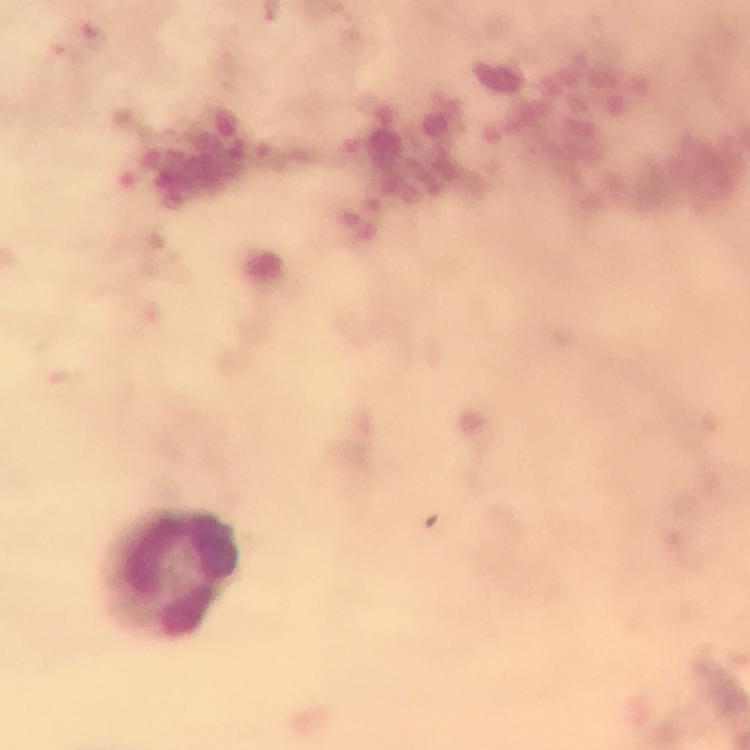
Approximate centers as (x, y) in pixels.
Summary:
  - Leukocyte locations: (172, 573)
  - Malaria parasites: none detected
  - Immersion oil: applied
  - Image size: 750×750 pixels
  - Preparation: thick blood film
  - Context: from a malaria diagnostic workup
  - Magnification: 100x
  - Capture: smartphone photograph through a microscope
  - Cropped from: one field of view
  - Stain: Giemsa